Identify the blood parasite species.
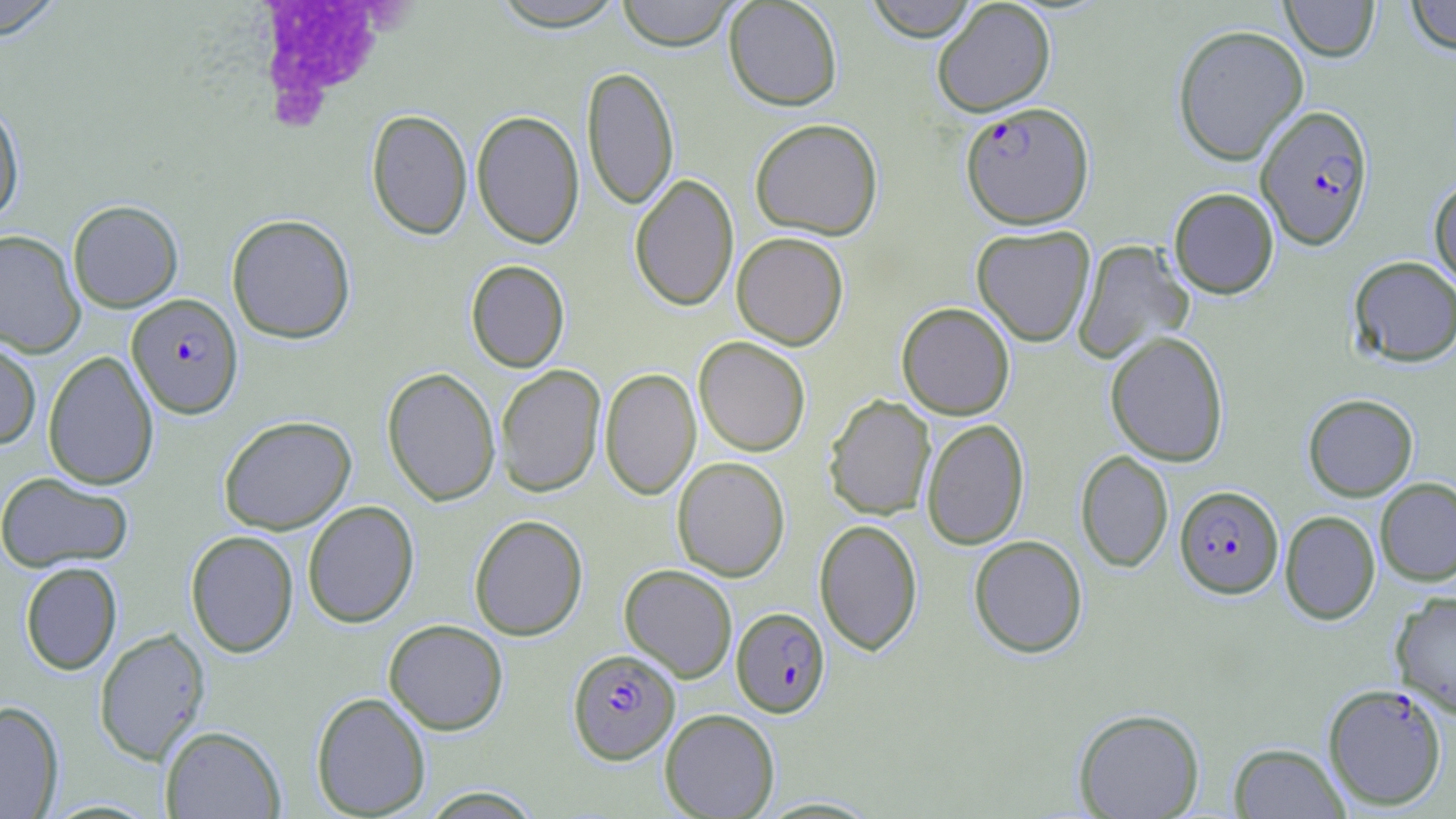
Plasmodium falciparum.

preparation: thin blood smear
plasmodium_falciparum_infected_red_blood_cell_locations: 'approximate bounding boxes as named x1/y1/x2/y2 corners in pixels: (x1=961, y1=101, x2=1094, y2=229), (x1=1255, y1=104, x2=1374, y2=250), (x1=127, y1=293, x2=243, y2=419), (x1=1175, y1=485, x2=1284, y2=598), (x1=731, y1=607, x2=830, y2=718), (x1=568, y1=648, x2=679, y2=764), (x1=1323, y1=683, x2=1448, y2=811)'
magnification: 1000x
uninfected_red_blood_cell_locations: 'approximate bounding boxes as named x1/y1/x2/y2 corners in pixels: (x1=0, y1=0, x2=65, y2=40), (x1=616, y1=0, x2=739, y2=51), (x1=723, y1=0, x2=843, y2=111), (x1=864, y1=0, x2=979, y2=41), (x1=932, y1=0, x2=1056, y2=117), (x1=1281, y1=0, x2=1380, y2=61), (x1=1405, y1=0, x2=1456, y2=55), (x1=488, y1=1, x2=631, y2=30), (x1=1172, y1=24, x2=1309, y2=166), (x1=582, y1=65, x2=679, y2=212), (x1=0, y1=97, x2=24, y2=224), (x1=366, y1=109, x2=472, y2=240), (x1=471, y1=110, x2=585, y2=249), (x1=750, y1=118, x2=883, y2=239), (x1=629, y1=174, x2=739, y2=312), (x1=1428, y1=177, x2=1456, y2=289), (x1=1168, y1=187, x2=1279, y2=298), (x1=68, y1=200, x2=183, y2=312), (x1=227, y1=214, x2=356, y2=343), (x1=971, y1=225, x2=1095, y2=347), (x1=0, y1=230, x2=85, y2=357), (x1=731, y1=232, x2=849, y2=349), (x1=1073, y1=239, x2=1195, y2=363), (x1=1348, y1=256, x2=1456, y2=367), (x1=465, y1=260, x2=569, y2=372), (x1=897, y1=302, x2=1015, y2=420), (x1=1105, y1=331, x2=1229, y2=466), (x1=0, y1=336, x2=41, y2=450), (x1=694, y1=336, x2=811, y2=456), (x1=43, y1=350, x2=159, y2=490), (x1=495, y1=364, x2=606, y2=497), (x1=382, y1=367, x2=501, y2=506), (x1=600, y1=367, x2=700, y2=500), (x1=1303, y1=394, x2=1418, y2=501), (x1=823, y1=395, x2=936, y2=520), (x1=218, y1=415, x2=356, y2=534), (x1=921, y1=419, x2=1029, y2=550), (x1=1075, y1=450, x2=1173, y2=573), (x1=672, y1=456, x2=790, y2=581), (x1=0, y1=471, x2=134, y2=573), (x1=1375, y1=477, x2=1456, y2=586), (x1=302, y1=500, x2=419, y2=628), (x1=1280, y1=510, x2=1380, y2=625), (x1=469, y1=514, x2=588, y2=640), (x1=814, y1=518, x2=922, y2=655), (x1=185, y1=530, x2=299, y2=658), (x1=969, y1=534, x2=1088, y2=658), (x1=20, y1=562, x2=122, y2=675), (x1=619, y1=564, x2=738, y2=682), (x1=1390, y1=591, x2=1456, y2=717), (x1=383, y1=619, x2=508, y2=735), (x1=94, y1=628, x2=210, y2=765), (x1=310, y1=691, x2=431, y2=818), (x1=0, y1=700, x2=64, y2=819), (x1=1073, y1=707, x2=1205, y2=819), (x1=660, y1=708, x2=780, y2=818), (x1=160, y1=725, x2=286, y2=818), (x1=1228, y1=742, x2=1349, y2=818), (x1=419, y1=786, x2=543, y2=818)'
image_size: 1456×819 pixels
field_of_view: single
stain: May-Grünwald-Giemsa
white_blood_cell_locations: 'approximate bounding boxes as named x1/y1/x2/y2 corners in pixels: (x1=241, y1=3, x2=417, y2=141)'
modality: optical microscopy